Report the malaria status of this cell.
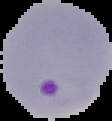
It is parasitized.

preparation = thin blood film
image type = cell region segmented out of the field of view; surrounding area masked to black
image size = 112×121 pixels